Classify this cell by malaria status.
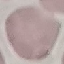

It is uninfected.

Summary:
  - Stain: Giemsa
  - Image type: cell patch, automatically extracted from a larger field of view and resized to 64 × 64 pixels
  - Preparation: thin blood smear
  - Capture: smartphone camera at the microscope eyepiece